Describe the morphology of the erythrocytes.
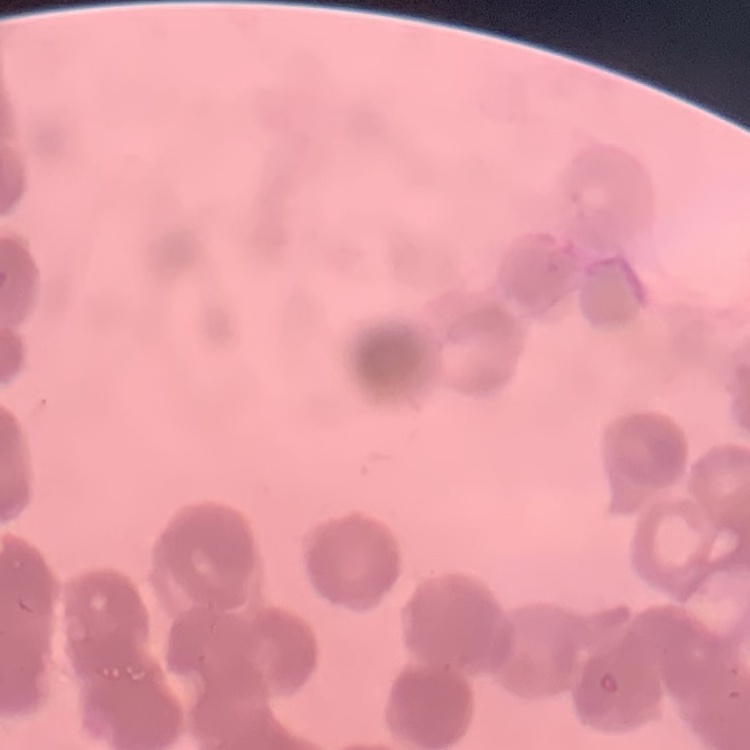
They show rouleaux formation.

Summary:
  - Image type: one tile cut from a larger photomicrograph
  - Preparation: thin blood film
  - Stain: Field's or Giemsa